Assess this cell for malaria.
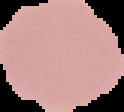

It is uninfected.

From a thin blood smear. Image is 124×112 pixels. Segmented cell region on a black background.